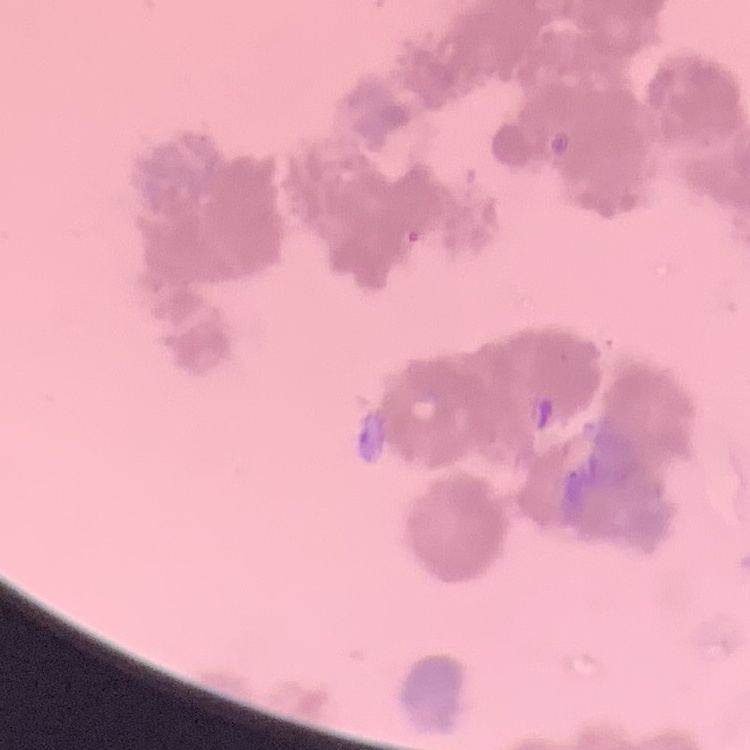
The erythrocytes exhibit rouleaux formation. Stained with either Field's or Giemsa. One tile cut from a larger photomicrograph. Thin peripheral smear.